Locate and identify every blood parasite.
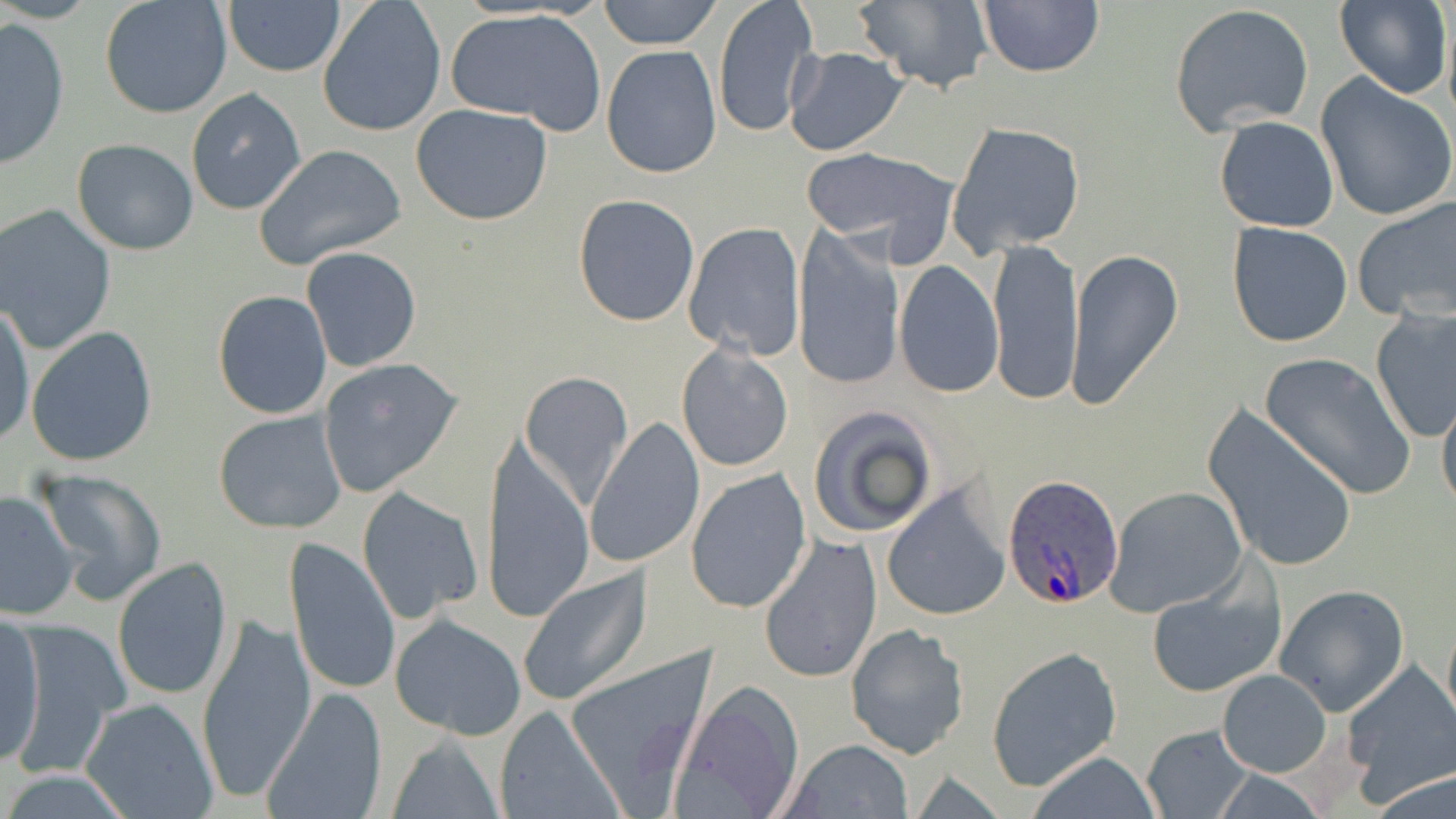

Approximate bounding boxes as (x1,y1)-(x2,y2) corner pairs in pixels.
Plasmodium ovale-infected red blood cells: (1003,474)-(1126,609).
No Plasmodium falciparum, Plasmodium malariae, Plasmodium vivax, Babesia divergens, or Trypanosoma brucei observed.

Uninfected red blood cell locations: (99,0)-(234,121), (222,0)-(345,78), (318,0)-(447,137), (600,0)-(722,50), (711,0)-(819,139), (853,0)-(994,92), (977,0)-(1106,76), (1335,0)-(1451,100), (1169,3)-(1315,135), (444,7)-(606,133), (0,17)-(70,168), (601,44)-(723,178), (784,46)-(908,156), (1315,74)-(1456,223), (186,88)-(308,214), (411,104)-(553,225), (1215,116)-(1338,233), (947,120)-(1086,258), (72,139)-(199,255), (253,144)-(406,269), (798,147)-(944,250), (572,193)-(702,327), (1353,194)-(1456,325), (0,205)-(117,355), (1227,222)-(1353,348), (683,223)-(806,361), (792,226)-(902,391), (987,237)-(1084,405), (300,246)-(421,373), (1065,248)-(1182,411), (896,259)-(1004,398), (213,291)-(333,420), (0,305)-(35,450), (1370,308)-(1456,444), (27,327)-(158,466), (677,344)-(793,473), (1259,353)-(1416,500), (317,357)-(462,497), (519,369)-(634,510), (1436,387)-(1456,518), (1201,401)-(1360,574), (806,403)-(942,541), (213,409)-(347,534), (585,418)-(706,569), (477,428)-(595,625), (32,469)-(167,605), (686,469)-(811,613), (882,485)-(1013,623), (358,486)-(483,623), (1105,486)-(1247,616), (1,490)-(78,620), (759,534)-(883,685), (282,538)-(401,699), (113,558)-(233,702), (518,567)-(653,708), (1145,577)-(1284,698), (1272,584)-(1409,716), (1442,613)-(1456,737), (1,614)-(44,768), (195,614)-(317,807), (390,615)-(527,740), (844,622)-(969,760), (6,623)-(129,775), (987,645)-(1123,792), (563,646)-(718,810), (1337,661)-(1456,799), (1216,669)-(1331,777), (671,680)-(804,817), (260,688)-(389,819), (80,698)-(218,819), (495,706)-(622,818), (1140,723)-(1255,818), (387,735)-(505,819), (782,739)-(914,818), (1024,750)-(1164,819), (1365,766)-(1456,819). Slide-level diagnosis: Plasmodium ovale. Thin blood smear. Captured at 1000x magnification. Light microscopy. Image is 1456×819 pixels. Single field of view. May-Grünwald-Giemsa-stained preparation.